Outline each blood parasite and name the species.
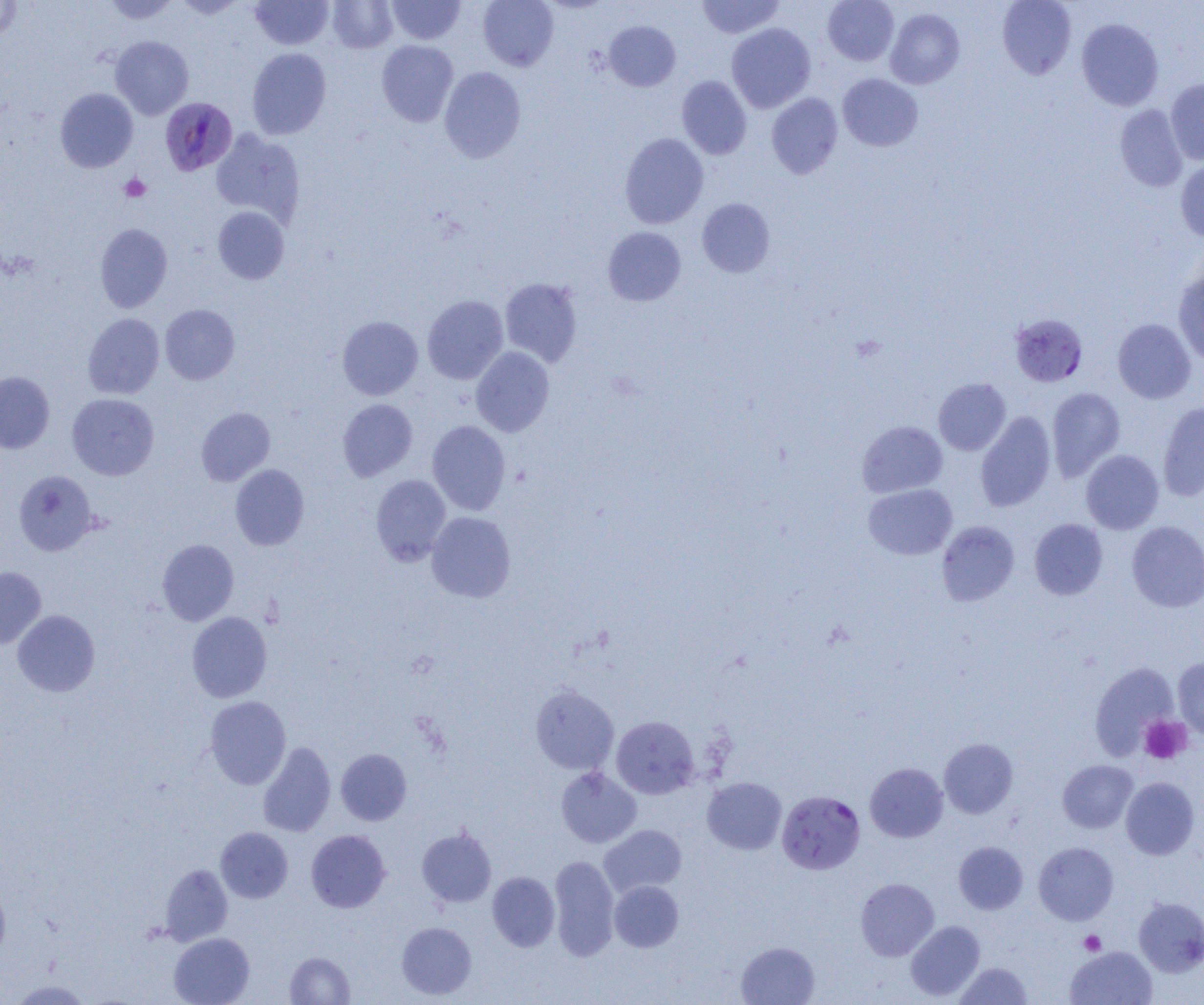

Approximate bounding boxes as (x1,y1)-(x2,y2) corner pairs in pixels.
Plasmodium falciparum-infected red blood cells: (160,97)-(238,176), (1009,313)-(1089,387), (777,790)-(865,874).
No Plasmodium ovale, Plasmodium malariae, Plasmodium vivax, Babesia divergens, or Trypanosoma brucei observed.

slide-level diagnosis = Plasmodium falciparum
platelet locations = approximate bounding boxes as (x1,y1)-(x2,y2) corner pairs in pixels: (119,173)-(151,202), (1139,715)-(1192,764), (1079,930)-(1106,955)
field of view = single
modality = light microscopy
image size = 1204×1005 pixels
magnification = 1000x
preparation = thin blood smear
uninfected red blood cell locations = approximate bounding boxes as (x1,y1)-(x2,y2) corner pairs in pixels: (104,0)-(179,25), (172,0)-(247,19), (251,0)-(334,49), (386,0)-(465,45), (478,0)-(559,71), (696,0)-(785,38), (823,0)-(899,66), (997,0)-(1077,80), (0,1)-(23,41), (327,1)-(397,53), (885,7)-(964,89), (1076,18)-(1164,111), (604,20)-(681,91), (726,23)-(816,112), (110,35)-(194,119), (377,40)-(458,127), (247,48)-(331,140), (439,66)-(526,163), (837,73)-(923,151), (676,76)-(751,159), (1165,78)-(1204,165), (55,88)-(138,172), (766,93)-(843,179), (1115,104)-(1188,192), (210,129)-(305,226), (620,133)-(709,229), (1176,158)-(1204,242), (697,198)-(775,278), (212,206)-(289,285), (95,223)-(173,313), (603,227)-(686,306), (1173,269)-(1204,366), (500,277)-(582,367), (422,295)-(508,384), (160,304)-(240,385), (83,313)-(165,399), (337,316)-(423,400), (1112,318)-(1196,404), (471,346)-(554,437), (0,371)-(55,453), (933,378)-(1011,455), (1046,387)-(1126,481), (67,393)-(159,480), (338,399)-(417,481), (1157,401)-(1204,502), (196,407)-(275,486), (975,411)-(1056,512), (427,420)-(511,515), (857,421)-(948,498), (1081,450)-(1164,534), (230,464)-(310,550), (14,471)-(98,556), (370,474)-(451,566), (863,484)-(957,560), (426,511)-(516,603), (1029,518)-(1108,600), (937,521)-(1019,606), (1127,521)-(1204,611), (157,539)-(239,625), (0,566)-(46,649), (12,609)-(100,697), (186,611)-(272,703), (1172,657)-(1204,739), (1091,663)-(1180,758), (530,685)-(619,774), (204,695)-(291,789), (611,716)-(699,799), (938,738)-(1018,819), (257,741)-(336,837), (336,748)-(411,825), (1057,759)-(1138,833), (864,763)-(948,842), (555,766)-(642,848), (702,777)-(787,854), (1120,777)-(1200,859), (599,824)-(687,898), (215,827)-(293,903), (416,827)-(496,908), (306,829)-(391,913), (1034,841)-(1118,924), (953,842)-(1028,914), (549,855)-(619,961), (159,863)-(233,946), (487,871)-(560,951), (0,877)-(11,962), (855,877)-(939,961), (609,881)-(683,952), (1134,896)-(1204,977), (905,920)-(985,1001), (396,921)-(477,1000), (169,932)-(255,1005), (736,941)-(820,1005), (1065,946)-(1157,1005), (285,952)-(355,1004), (954,961)-(1033,1004), (8,978)-(92,1004)